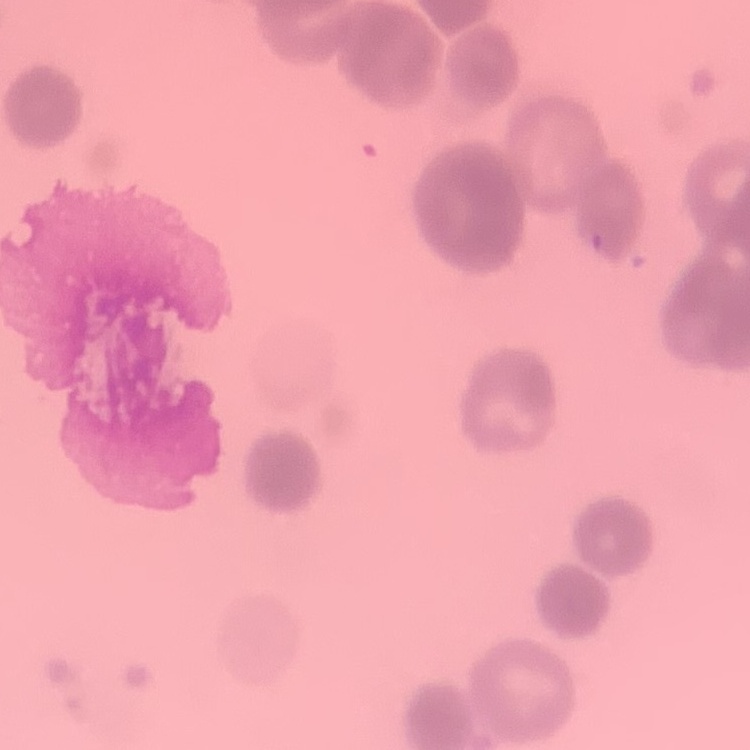 The red blood cells exhibit rouleaux formation. Thin blood film. Square crop of a larger photomicrograph. Field's or Giemsa stain.